Identify the parasite.
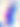

This is Toxoplasma gondii.

Captured at 400x magnification. Micrograph.